Comment on the morphology of the red blood cells.
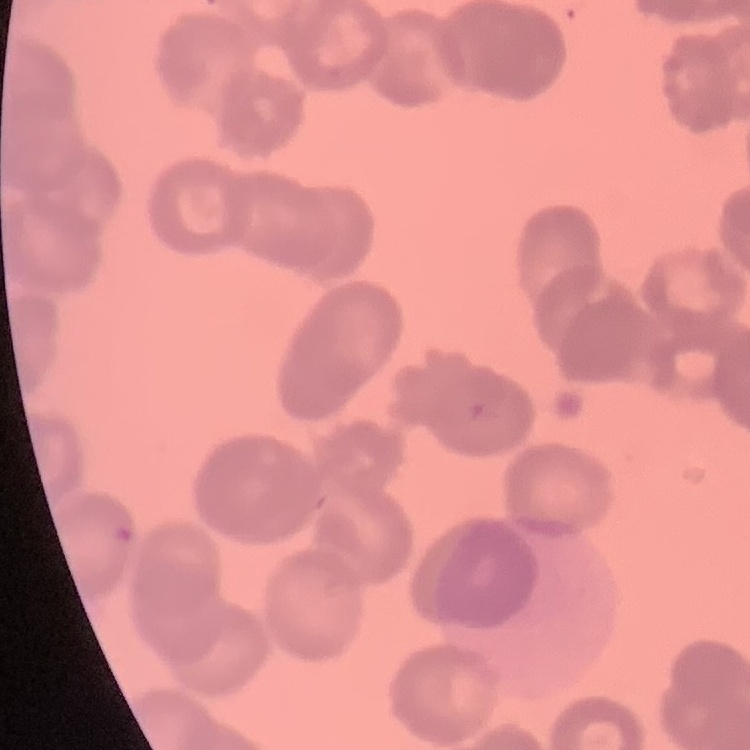

They show rouleaux formation.

Thin blood smear. One tile cut from a larger photomicrograph. Stained with either Field's or Giemsa.